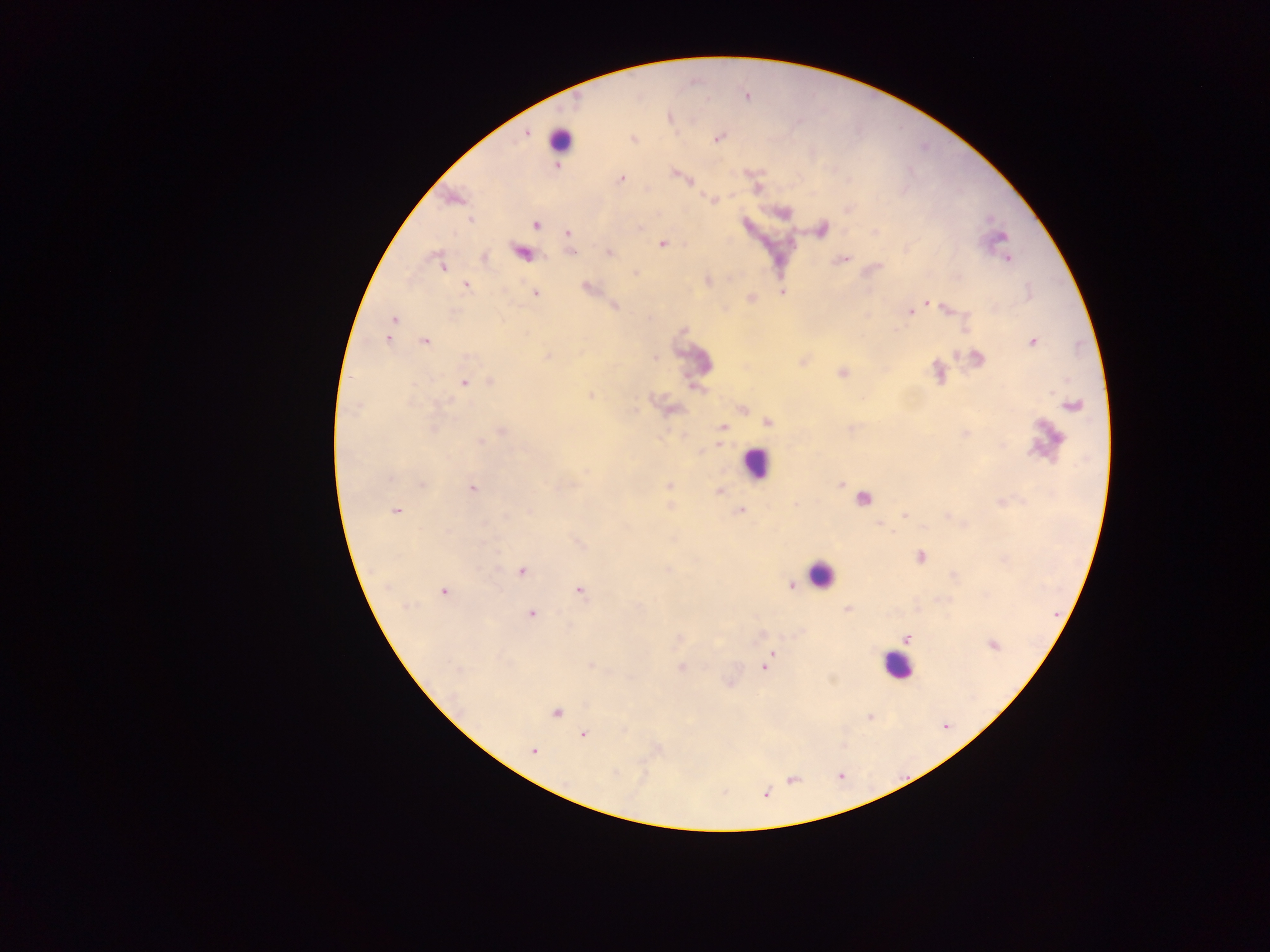 Approximate centers as {x, y} in pixels. Leukocyte locations: {560, 140}, {756, 463}, {820, 574}, {896, 666}. Plasmodium parasite locations: {525, 131}, {718, 138}, {631, 139}, {558, 165}, {676, 173}, {621, 179}, {453, 198}, {713, 199}, {471, 218}, {536, 224}, {822, 228}, {874, 232}, {567, 233}, {662, 243}, {521, 251}, {571, 251}, {608, 252}, {484, 258}, {1007, 258}, {841, 259}, {440, 264}, {635, 273}, {708, 281}, {465, 284}, {586, 287}, {782, 292}, {535, 293}, {750, 298}, {925, 303}, {613, 306}, {916, 307}, {946, 307}, {908, 312}, {393, 320}, {390, 329}, {388, 337}, {425, 341}, {1032, 341}, {548, 355}, {654, 357}, {975, 359}, {842, 373}, {937, 373}, {491, 382}, {464, 383}, {591, 395}, {1072, 405}, {742, 409}, {766, 422}, {722, 426}, {502, 431}, {479, 440}, {719, 443}, {422, 484}, {669, 485}, {840, 485}, {471, 488}, {718, 491}, {862, 497}, {1001, 502}, {740, 510}, {396, 511}, {904, 516}, {579, 543}, {920, 557}, {521, 571}, {790, 584}, {578, 590}, {443, 591}, {846, 609}, {530, 613}, {906, 638}, {677, 639}, {993, 644}, {771, 654}, {590, 664}, {766, 666}, {681, 668}, {556, 712}, {869, 716}, {583, 735}, {533, 750}, {766, 794}. Collected in Ghana. Image is 1270×952 pixels. One field of view. Thick blood film. Mobile-phone photograph taken through the microscope.